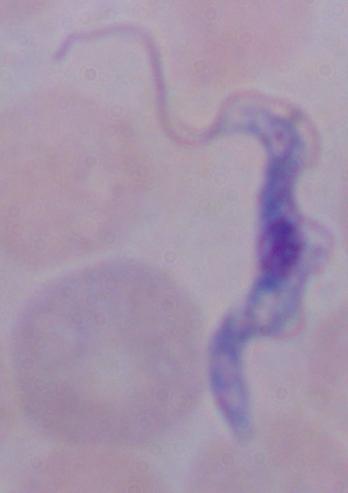

Summary:
  - Modality: micrograph
  - Magnification: 1000x
  - Identification: trypanosome